Classify this cell by malaria status.
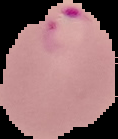

Parasitized.

From a thin blood smear. Image is 118×139 pixels. Segmented cell region on a black background.